Assess the morphology of the erythrocytes.
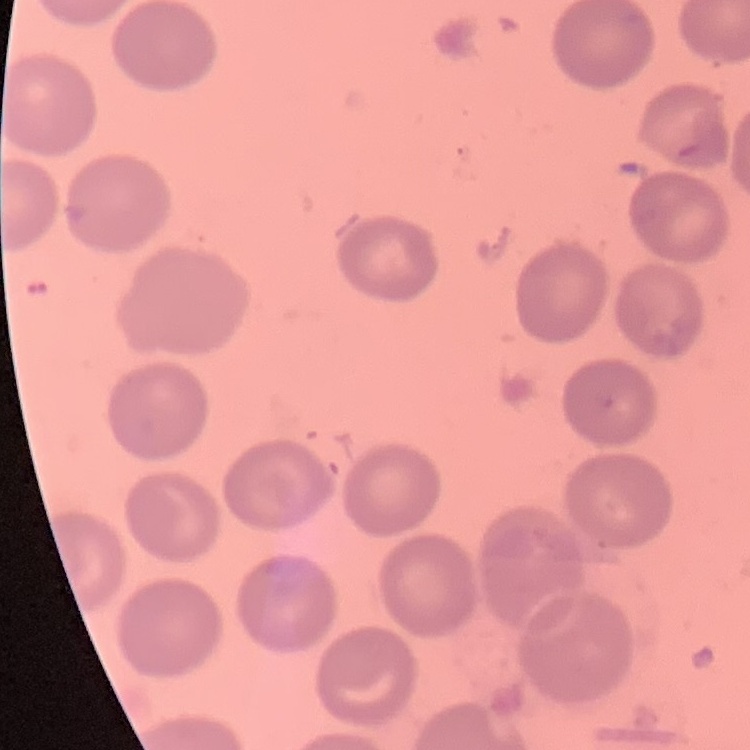

No rouleaux formation.

Summary:
  - Preparation: thin blood film
  - Image type: square crop of a larger photomicrograph
  - Stain: Field's or Giemsa